Locate malaria parasites and leukocytes.
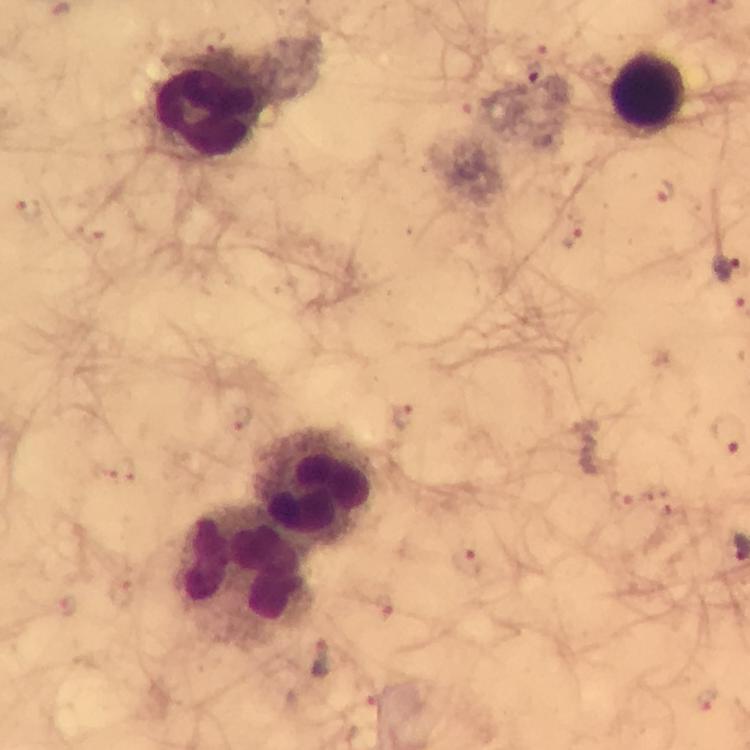

Approximate centers as [x, y] in pixels.
Malaria parasites: [535, 72], [665, 194], [29, 207], [573, 239], [725, 264], [403, 416], [728, 432], [124, 470], [622, 501], [467, 562], [121, 590], [65, 605], [384, 605], [322, 661], [707, 700].
Leukocytes: [647, 94], [206, 112], [315, 484], [243, 573].

cropped from = a single field of view
stain = Giemsa
image size = 750×750 pixels
immersion oil = used
preparation = thick blood film
context = from a diagnostic examination for malaria
capture = smartphone camera through the microscope
magnification = 100x